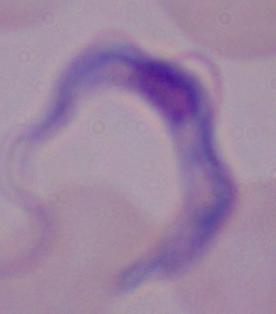
Summary:
  - Modality: photomicrograph
  - Identification: trypanosome
  - Magnification: 1000x